Report the malaria status of this cell.
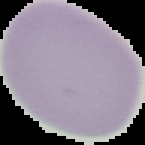

Uninfected.

Summary:
  - Image size: 145×145 pixels
  - Preparation: thin blood film
  - Image type: segmented cell region with the area outside set to black